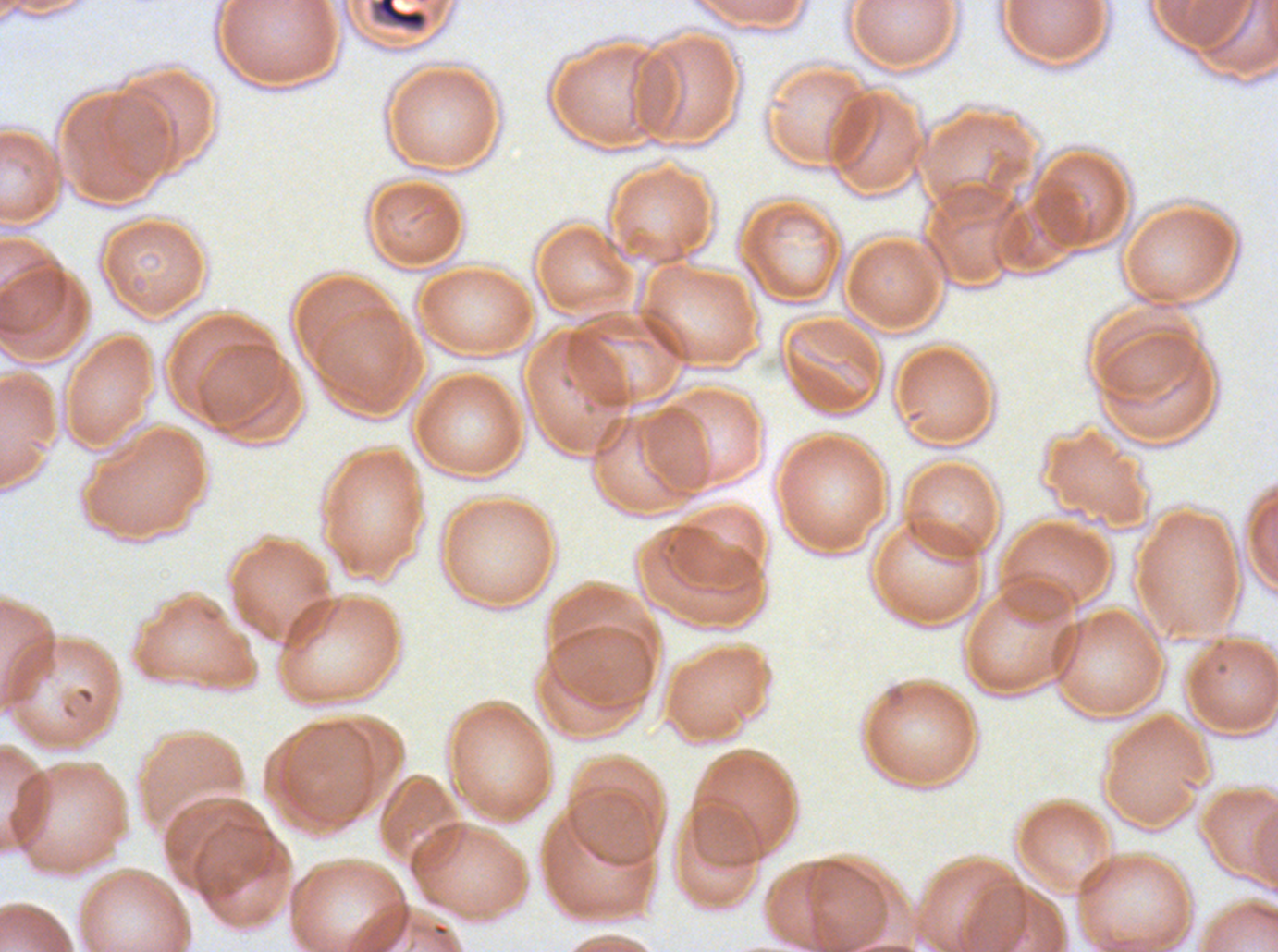
notation = approximate bounding boxes as {x1, y1, x2, y2} in pixels
debris locations = {366, 0, 432, 35}
specimen = P. falciparum from a patient in The Gambia, cultured ex vivo for 24 to 48 hours
field of view = one sub-image of a larger composite
preparation = thin blood smear
stain = Giemsa
image size = 1278×952 pixels